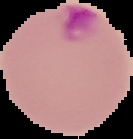 Cell region segmented out of the field of view; the surrounding area is masked to black. From a thin blood smear. Malaria status: parasitized. Image is 133×139 pixels.